Identify the blood parasite species.
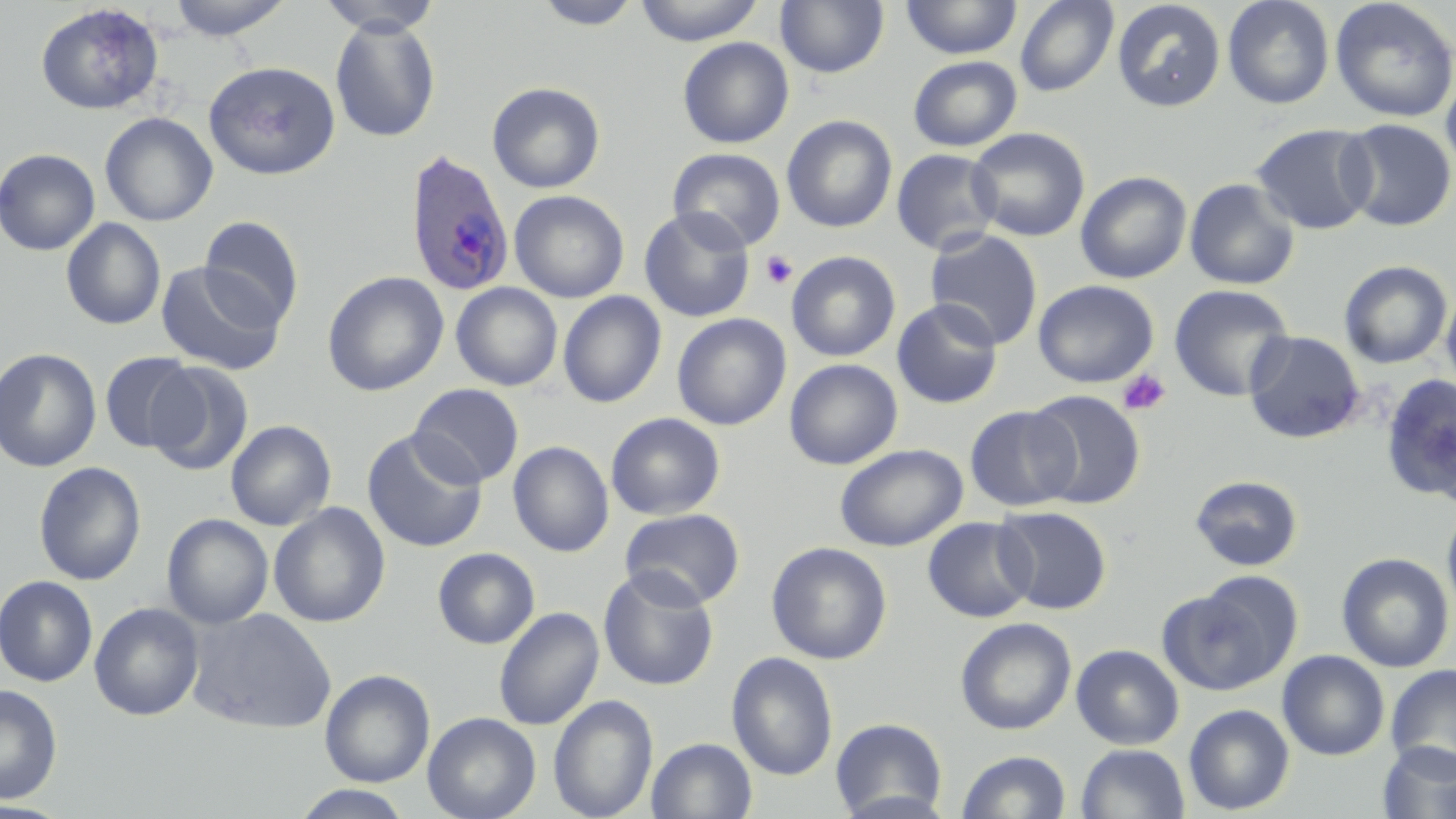

Plasmodium ovale.

Approximate bounding boxes as (x1, y1, x2, y2) in pixels. Plasmodium ovale-infected red blood cell locations: (403, 148, 515, 296). Uninfected red blood cell locations: (167, 0, 294, 40), (317, 0, 441, 37), (633, 0, 765, 46), (775, 0, 890, 79), (901, 0, 1022, 59), (1222, 0, 1336, 110), (1329, 0, 1456, 123), (532, 1, 643, 30), (1015, 1, 1119, 97), (1112, 1, 1226, 113), (35, 3, 163, 115), (330, 18, 441, 142), (677, 37, 794, 148), (908, 55, 1022, 152), (203, 61, 341, 179), (1440, 71, 1456, 181), (487, 81, 605, 193), (100, 112, 218, 226), (782, 115, 898, 233), (1337, 119, 1455, 231), (1251, 123, 1378, 235), (967, 127, 1090, 242), (667, 147, 786, 252), (0, 148, 101, 256), (891, 148, 1002, 255), (1075, 171, 1192, 284), (1184, 178, 1301, 290), (509, 190, 629, 303), (639, 207, 755, 322), (199, 215, 304, 327), (61, 218, 166, 330), (924, 228, 1044, 350), (786, 251, 901, 361), (1338, 260, 1453, 368), (155, 261, 287, 376), (322, 271, 449, 396), (1032, 280, 1159, 387), (451, 282, 563, 392), (1169, 284, 1295, 402), (1441, 287, 1456, 398), (557, 291, 667, 408), (891, 297, 1003, 409), (672, 313, 791, 430), (1243, 331, 1365, 444), (0, 347, 102, 473), (99, 351, 201, 453), (784, 359, 903, 470), (145, 361, 254, 476), (1379, 374, 1456, 503), (409, 383, 524, 487), (1025, 389, 1146, 508), (964, 405, 1082, 512), (606, 412, 726, 520), (225, 420, 336, 531), (363, 430, 488, 553), (509, 440, 614, 557), (835, 444, 967, 551), (33, 462, 146, 586), (1189, 475, 1303, 572), (268, 502, 391, 627), (1441, 502, 1456, 625), (993, 506, 1112, 615), (620, 508, 745, 609), (162, 513, 274, 629), (922, 517, 1037, 622), (766, 541, 892, 664), (432, 547, 540, 649), (1336, 552, 1454, 672), (598, 566, 719, 691), (1171, 571, 1304, 691), (0, 575, 98, 686), (89, 602, 204, 721), (187, 607, 336, 734), (493, 607, 605, 731), (955, 617, 1076, 735), (1071, 644, 1185, 749), (1277, 650, 1390, 761), (726, 652, 838, 780), (1385, 664, 1456, 775), (320, 669, 435, 787), (0, 684, 62, 805), (549, 695, 658, 819), (1183, 704, 1295, 815), (422, 711, 541, 819), (830, 717, 948, 818), (646, 737, 758, 819), (1377, 741, 1456, 819), (1076, 743, 1190, 819), (956, 750, 1071, 818), (290, 786, 416, 819). Platelet locations: (760, 250, 799, 289), (1118, 369, 1171, 416). Captured at 1000x magnification. Thin blood film. May-Grünwald-Giemsa-stained preparation. Light microscopy. Image is 1456×819 pixels. Single field of view.